Name the parasite shown.
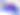

This is Toxoplasma gondii.

Photomicrograph. Captured at 400x magnification.